Classify this cell by malaria status.
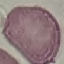

It is uninfected.

{
  "stain": "Giemsa",
  "capture": "smartphone camera at the microscope eyepiece",
  "image_type": "automatically extracted cell patch, resized to 64 × 64 pixels",
  "preparation": "thin blood smear"
}